Report the malaria status of this cell.
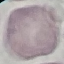

Uninfected.

Cell patch, automatically extracted from a larger field of view and resized to 64 × 64 pixels. Acquired by smartphone through the microscope eyepiece. Giemsa stain. Thin blood film.